Describe the morphology of the red blood cells.
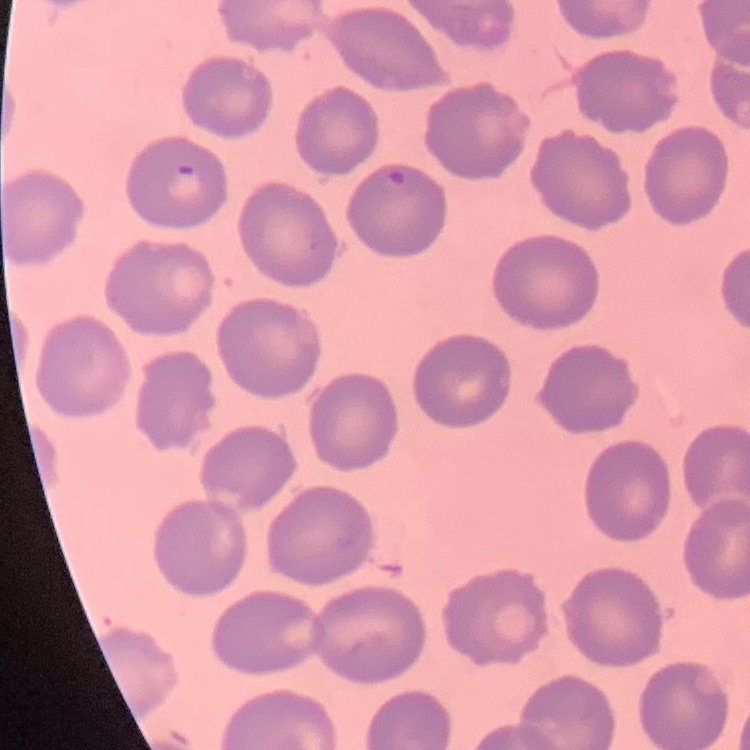
They show no rouleaux formation.

stain = Field's or Giemsa
image type = one tile cut from a larger photomicrograph
preparation = thin blood film